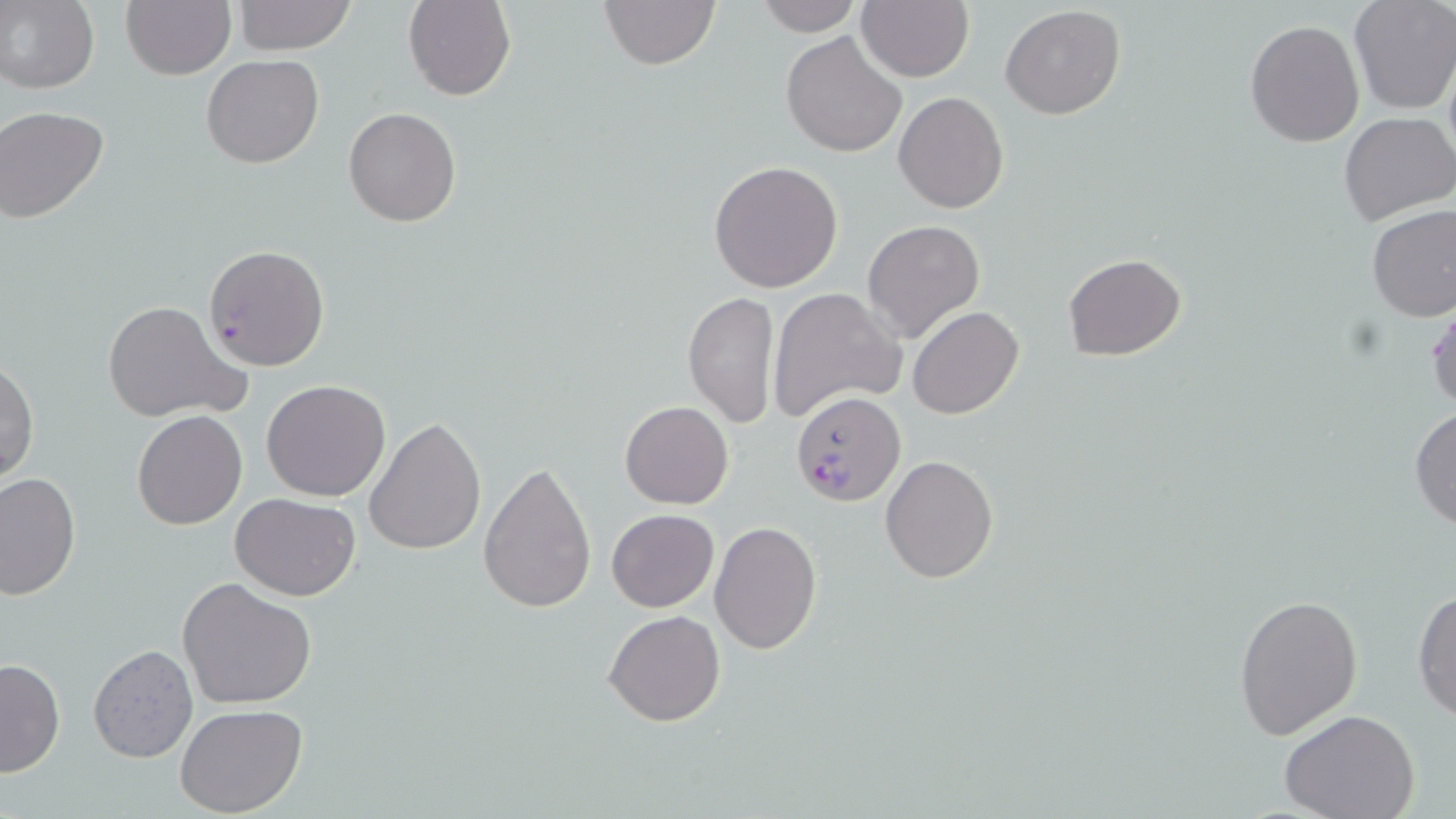

Approximate bounding boxes as (x1, y1, x2, y2) in pixels. Plasmodium falciparum-infected red blood cell locations: (203, 243, 331, 370), (792, 392, 906, 506). Uninfected red blood cell locations: (0, 0, 99, 93), (120, 0, 235, 80), (597, 0, 722, 72), (752, 0, 864, 36), (230, 1, 357, 54), (403, 1, 516, 101), (1348, 1, 1455, 115), (857, 2, 973, 81), (999, 5, 1126, 119), (1244, 20, 1365, 148), (780, 32, 907, 158), (1443, 51, 1456, 170), (200, 54, 324, 168), (894, 92, 1009, 212), (1, 105, 113, 225), (343, 107, 461, 227), (1338, 112, 1455, 227), (708, 160, 843, 293), (1365, 205, 1456, 321), (861, 219, 985, 342), (1063, 254, 1185, 360), (766, 287, 907, 423), (683, 290, 780, 428), (1427, 296, 1456, 413), (101, 301, 251, 424), (907, 305, 1025, 420), (1, 357, 38, 485), (260, 380, 391, 502), (619, 401, 734, 510), (1408, 405, 1456, 532), (132, 410, 247, 529), (365, 418, 486, 557), (880, 454, 999, 584), (479, 459, 598, 612), (0, 471, 80, 600), (231, 493, 362, 602), (605, 508, 719, 612), (708, 521, 822, 655), (177, 576, 316, 707), (1413, 586, 1456, 726), (1233, 593, 1364, 740), (604, 609, 726, 728), (87, 646, 198, 763), (0, 657, 65, 778), (175, 703, 308, 817), (1281, 710, 1421, 819). Slide-level diagnosis: Plasmodium falciparum. Optical microscopy. May-Grünwald-Giemsa-stained preparation. Thin blood film. Image is 1456×819 pixels. Single field of view. Captured at 1000x magnification.